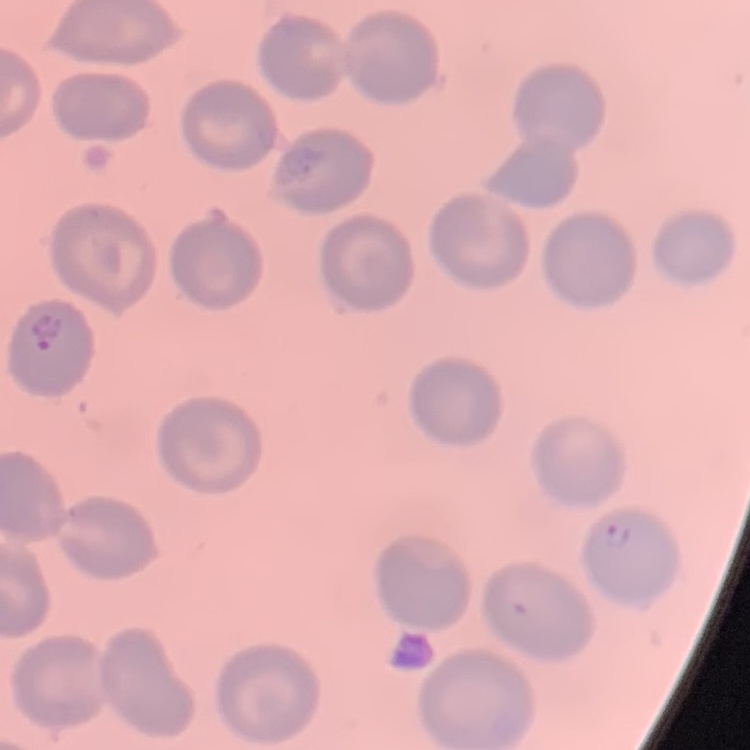

red blood cell morphology = no rouleaux formation
preparation = thin peripheral smear
image type = one tile cut from a larger photomicrograph
stain = Field's or Giemsa